Classify this cell by malaria status.
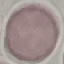

It is uninfected.

Thin blood smear. Acquired by smartphone through the microscope eyepiece. Giemsa stain. Automatically extracted cell patch, resized to 64 × 64 pixels.